Point out every Plasmodium parasite and every leukocyte.
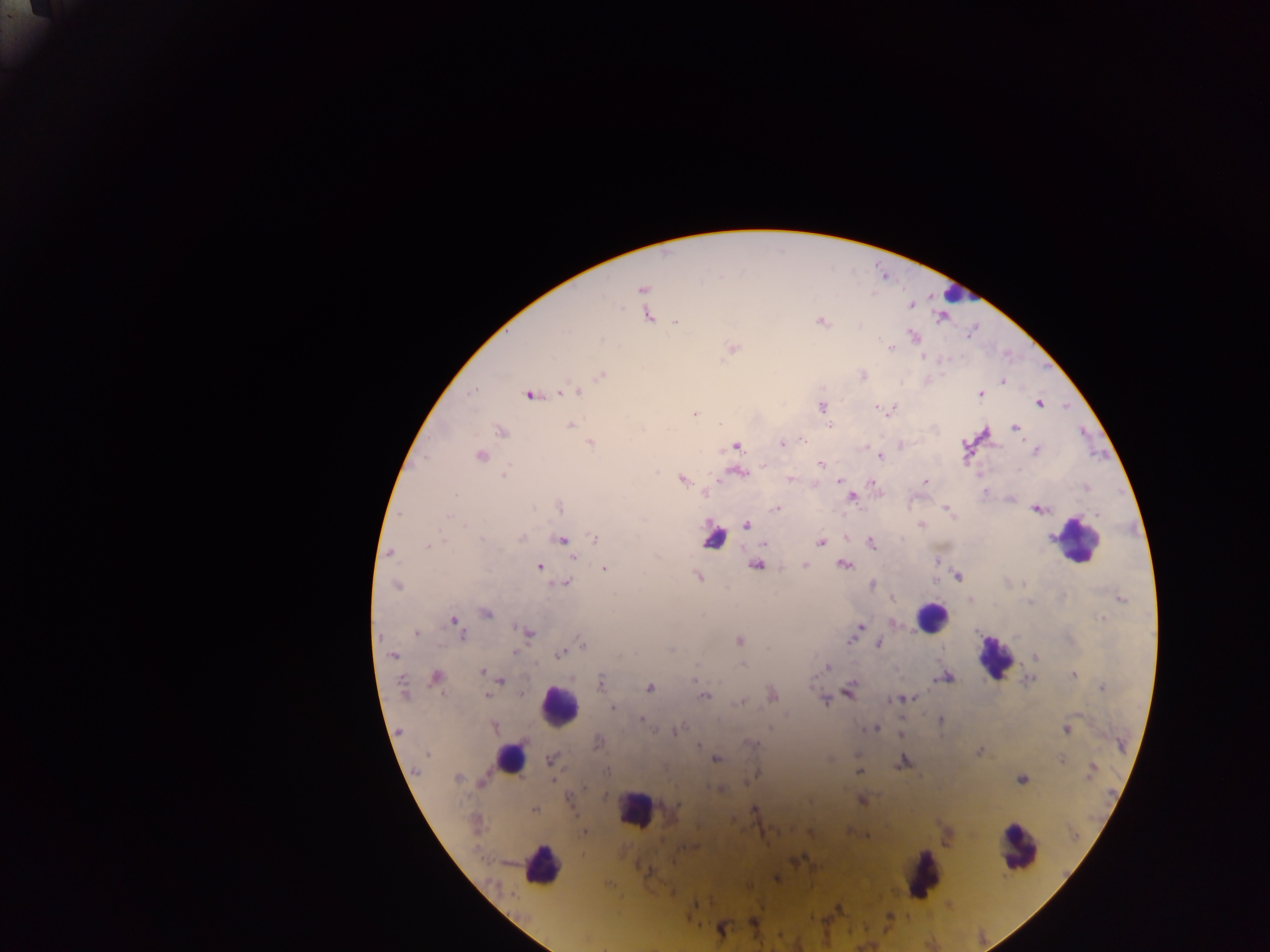

Approximate centers as (x, y) in pixels.
Plasmodium parasites: (642, 289), (910, 304), (648, 316), (675, 322), (822, 322), (914, 335), (602, 340), (733, 348), (891, 348), (923, 357), (601, 375), (862, 375), (1004, 382), (473, 391), (565, 391), (576, 391), (530, 395), (980, 395), (1039, 403), (821, 407), (876, 408), (891, 410), (694, 414), (570, 425), (1015, 426), (501, 431), (803, 440), (590, 444), (783, 444), (736, 446), (1036, 451), (480, 455), (879, 456), (821, 465), (738, 473), (505, 475), (682, 479), (790, 479), (839, 481), (926, 481), (873, 483), (851, 497), (559, 507), (533, 508), (777, 508), (947, 509), (1039, 509), (447, 516), (465, 523), (747, 525), (922, 525), (595, 538), (521, 539), (561, 539), (481, 540), (445, 541), (820, 542), (872, 543), (764, 544), (427, 546), (390, 553), (573, 558), (844, 564), (756, 565), (804, 565), (539, 567), (603, 568), (698, 576), (957, 576), (566, 583), (396, 585), (872, 585), (1121, 598), (894, 599), (1030, 602), (486, 612), (1102, 619), (454, 620), (860, 627), (417, 633), (527, 633), (462, 636), (851, 640), (740, 641), (879, 642), (582, 643), (515, 652), (560, 654), (393, 655), (1036, 657), (742, 665), (828, 666), (482, 672), (1073, 675), (436, 676), (694, 676), (946, 678), (500, 680), (1029, 680), (600, 683), (1102, 687), (650, 688), (403, 689), (849, 690), (520, 694), (772, 695), (487, 696), (703, 696), (906, 698), (824, 700), (738, 703), (612, 707), (641, 718), (940, 720), (493, 727), (679, 728), (874, 729), (676, 730), (1066, 730), (900, 734), (599, 742), (698, 745), (753, 745), (979, 751), (427, 754), (550, 759), (716, 759), (829, 760), (1062, 760), (902, 762), (605, 771), (1091, 771), (858, 772), (757, 773), (456, 778), (1021, 779), (553, 780), (570, 799), (862, 800), (809, 801), (754, 809), (534, 810), (584, 833), (649, 872), (776, 877), (753, 921), (720, 928).
Leukocytes: (954, 293), (714, 536), (1077, 536), (931, 617), (994, 656), (558, 705), (511, 758), (636, 809), (1017, 848), (537, 862), (923, 875).

preparation = thick blood smear
field of view = single
country = Ghana
image size = 1270×952 pixels
capture = mobile-phone photograph through a microscope